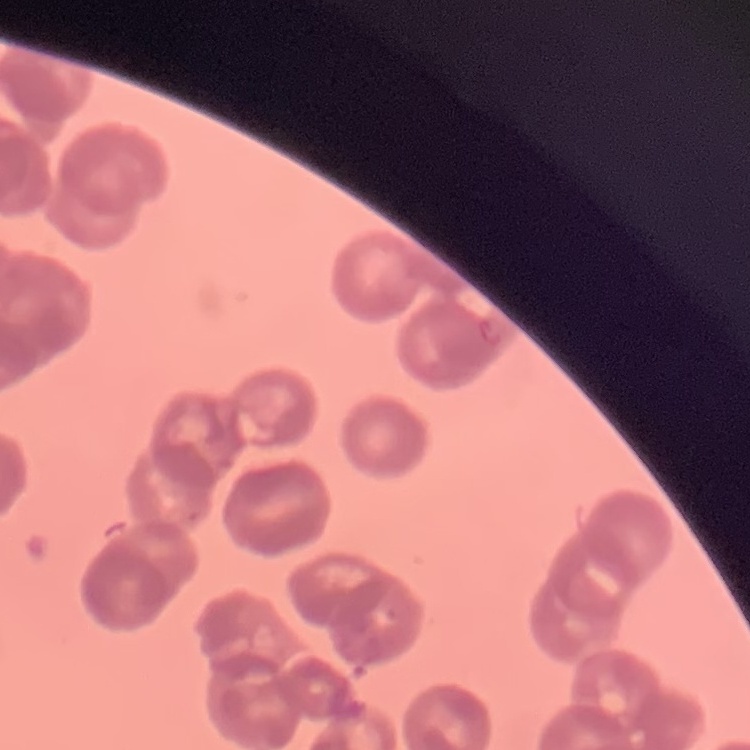
The red blood cells exhibit rouleaux formation. One tile cut from a larger photomicrograph. Stained with either Field's or Giemsa. Thin blood smear.